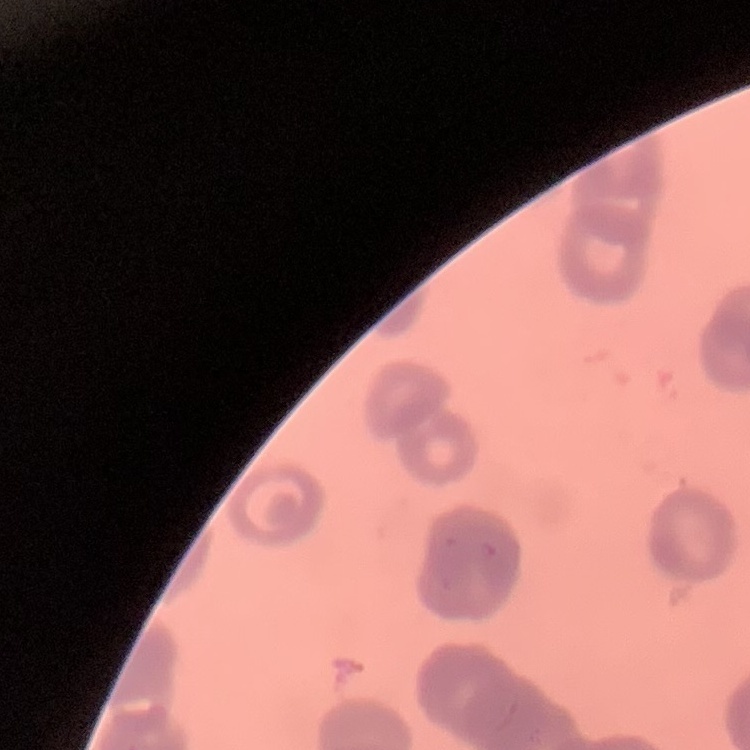

red blood cell morphology = rouleaux formation
preparation = thin blood film
image type = square crop of a larger photomicrograph
stain = Field's or Giemsa